Locate every blood parasite and identify its species.
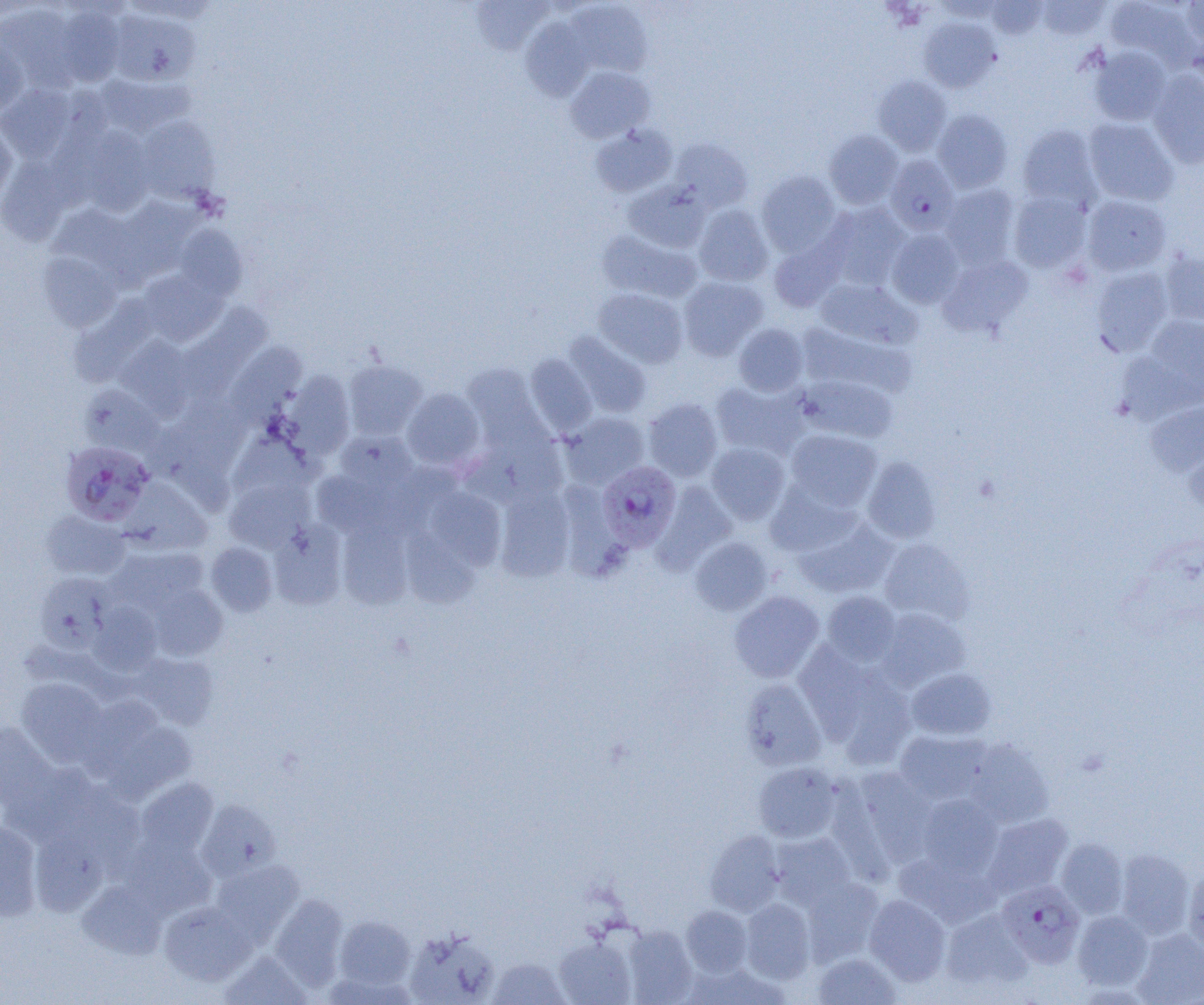
Approximate bounding boxes as (x1,y1)-(x2,y2) corner pairs in pixels.
Plasmodium falciparum-infected red blood cells: (885,155)-(959,235), (60,441)-(154,526), (597,461)-(681,550), (996,880)-(1085,968).
No Plasmodium ovale, Plasmodium malariae, Plasmodium vivax, Babesia divergens, or Trypanosoma brucei observed.

slide-level diagnosis = Plasmodium falciparum
preparation = thin blood film
magnification = 1000x
image size = 1204×1005 pixels
uninfected red blood cell locations = approximate bounding boxes as (x1,y1)-(x2,y2) corner pairs in pixels: (471,0)-(554,55), (1036,0)-(1110,40), (1106,0)-(1199,71), (986,1)-(1047,39), (0,2)-(42,20), (568,2)-(652,78), (1181,2)-(1204,55), (0,3)-(80,88), (55,5)-(126,87), (108,9)-(201,87), (520,18)-(594,101), (920,18)-(1000,92), (0,39)-(28,116), (1088,45)-(1172,126), (564,65)-(654,143), (1147,71)-(1204,167), (97,74)-(193,136), (873,75)-(952,155), (0,83)-(77,163), (932,109)-(1012,192), (136,116)-(219,203), (1083,118)-(1178,206), (0,121)-(17,209), (590,123)-(677,197), (1017,124)-(1102,209), (77,125)-(154,216), (824,130)-(903,209), (670,139)-(753,212), (0,156)-(70,246), (756,171)-(841,256), (623,180)-(711,252), (939,183)-(1021,268), (1009,192)-(1092,273), (1081,195)-(1171,276), (114,197)-(200,280), (821,202)-(910,288), (49,203)-(137,275), (693,204)-(773,286), (174,225)-(247,301), (886,228)-(964,308), (597,230)-(701,303), (769,235)-(846,312), (38,251)-(122,332), (1159,251)-(1204,325), (938,255)-(1032,336), (1091,267)-(1174,356), (139,268)-(228,346), (678,276)-(768,360), (815,278)-(920,349), (593,288)-(687,368), (68,296)-(157,387), (177,304)-(271,403), (1139,315)-(1204,402), (734,323)-(808,396), (796,323)-(914,397), (563,331)-(652,418), (115,336)-(196,421), (226,343)-(306,426), (525,353)-(597,435), (344,360)-(427,439), (462,364)-(545,446), (284,372)-(355,459), (797,374)-(898,443), (710,379)-(809,460), (81,385)-(163,457), (402,388)-(484,470), (168,398)-(250,479), (642,398)-(723,481), (1145,400)-(1204,476), (561,412)-(649,489), (785,429)-(882,511), (336,431)-(416,494), (460,433)-(564,508), (706,442)-(790,524), (1184,442)-(1204,516), (862,457)-(940,543), (312,470)-(394,537), (225,478)-(312,552), (120,480)-(212,554), (653,481)-(737,574), (766,481)-(861,557), (427,487)-(506,569), (495,487)-(575,581), (41,511)-(130,580), (794,517)-(897,599), (338,519)-(412,609), (270,522)-(347,610), (401,527)-(479,609), (689,537)-(773,616), (879,539)-(974,625), (205,542)-(278,616), (108,546)-(208,613), (35,573)-(114,654), (149,584)-(227,660), (729,591)-(824,682), (822,591)-(901,666), (89,602)-(162,676), (876,607)-(970,691), (794,643)-(879,740), (130,653)-(218,730), (906,668)-(996,740), (831,670)-(915,769), (16,677)-(108,766), (740,678)-(827,771), (81,694)-(177,783), (97,719)-(197,802), (0,722)-(59,812), (894,730)-(990,805), (964,739)-(1054,828), (753,762)-(842,843), (853,768)-(936,865), (136,778)-(218,856), (917,795)-(1003,879), (196,800)-(281,881), (982,813)-(1073,899), (0,821)-(42,920), (29,829)-(107,916), (705,830)-(785,915), (770,833)-(856,908), (119,835)-(216,919), (1056,838)-(1129,920), (1115,849)-(1194,938), (894,853)-(999,929), (211,859)-(305,944), (1183,869)-(1204,955), (803,877)-(883,963), (77,881)-(167,959), (270,894)-(348,991), (864,894)-(951,985), (740,898)-(815,984), (159,901)-(256,986), (681,906)-(752,977), (941,909)-(1032,991), (1072,910)-(1154,991), (334,916)-(415,991), (623,925)-(697,1004), (405,929)-(499,1005), (1132,929)-(1204,1005), (554,935)-(635,1005), (219,950)-(312,1005), (813,952)-(901,1005), (488,958)-(570,1004), (686,962)-(790,1004)
field of view = single
modality = light microscopy